Locate every Plasmodium parasite.
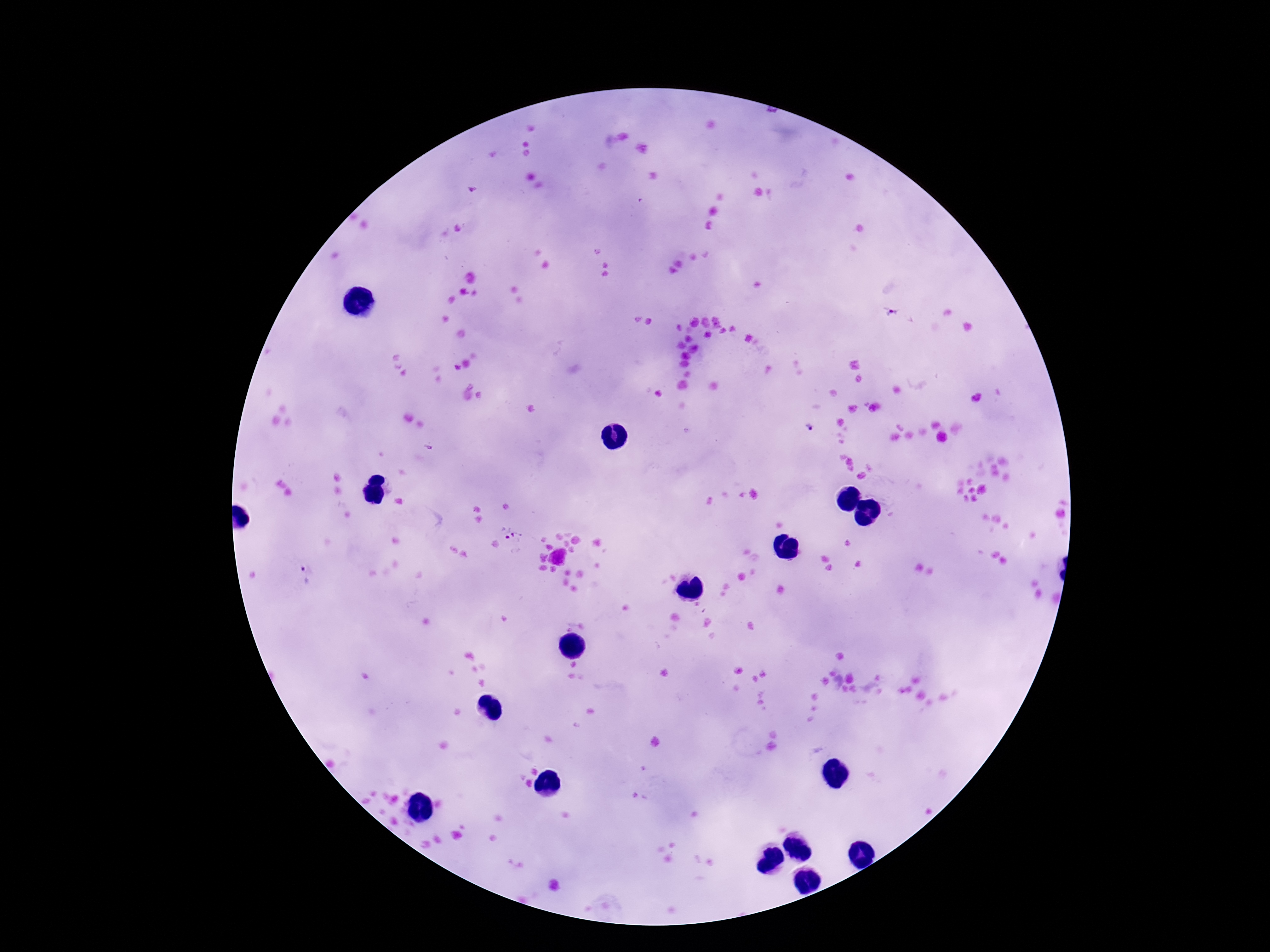

Approximate object centers, in pixels from the top-left corner.
Plasmodium parasites: (x=893, y=312), (x=809, y=427), (x=514, y=534), (x=305, y=575).

patient malaria status = positive
magnification = 100x
preparation = thick blood smear
stain = Giemsa
image size = 1270×952 pixels
field of view = single
capture = smartphone camera through the microscope eyepiece